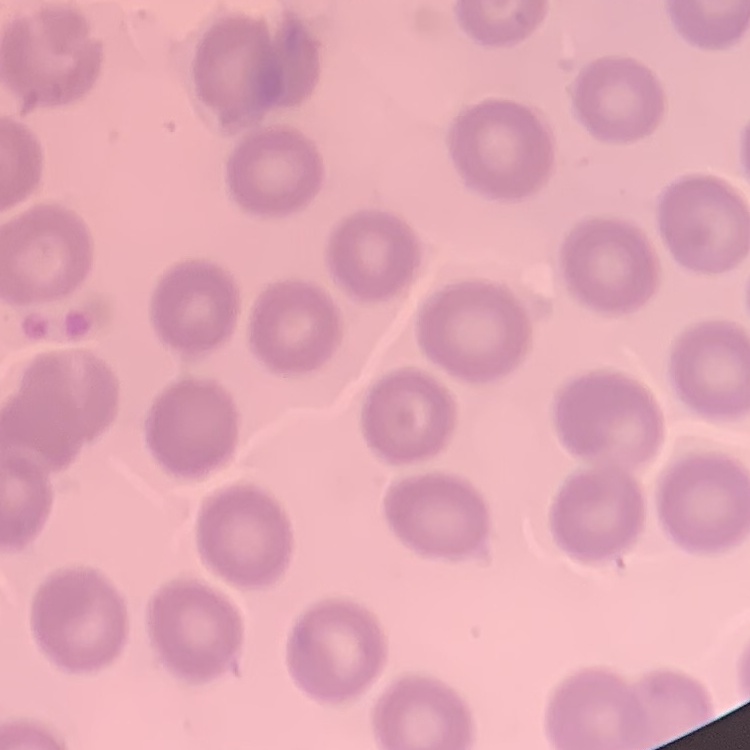 The red blood cells show no rouleaux formation. Stained with either Field's or Giemsa. One tile cut from a larger photomicrograph. Thin blood film.